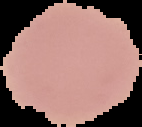

Cell region segmented out of the field of view; the surrounding area is masked to black. Image is 142×127 pixels. From a thin blood film. Result: no malaria parasites detected.